Assess for Plasmodium parasites.
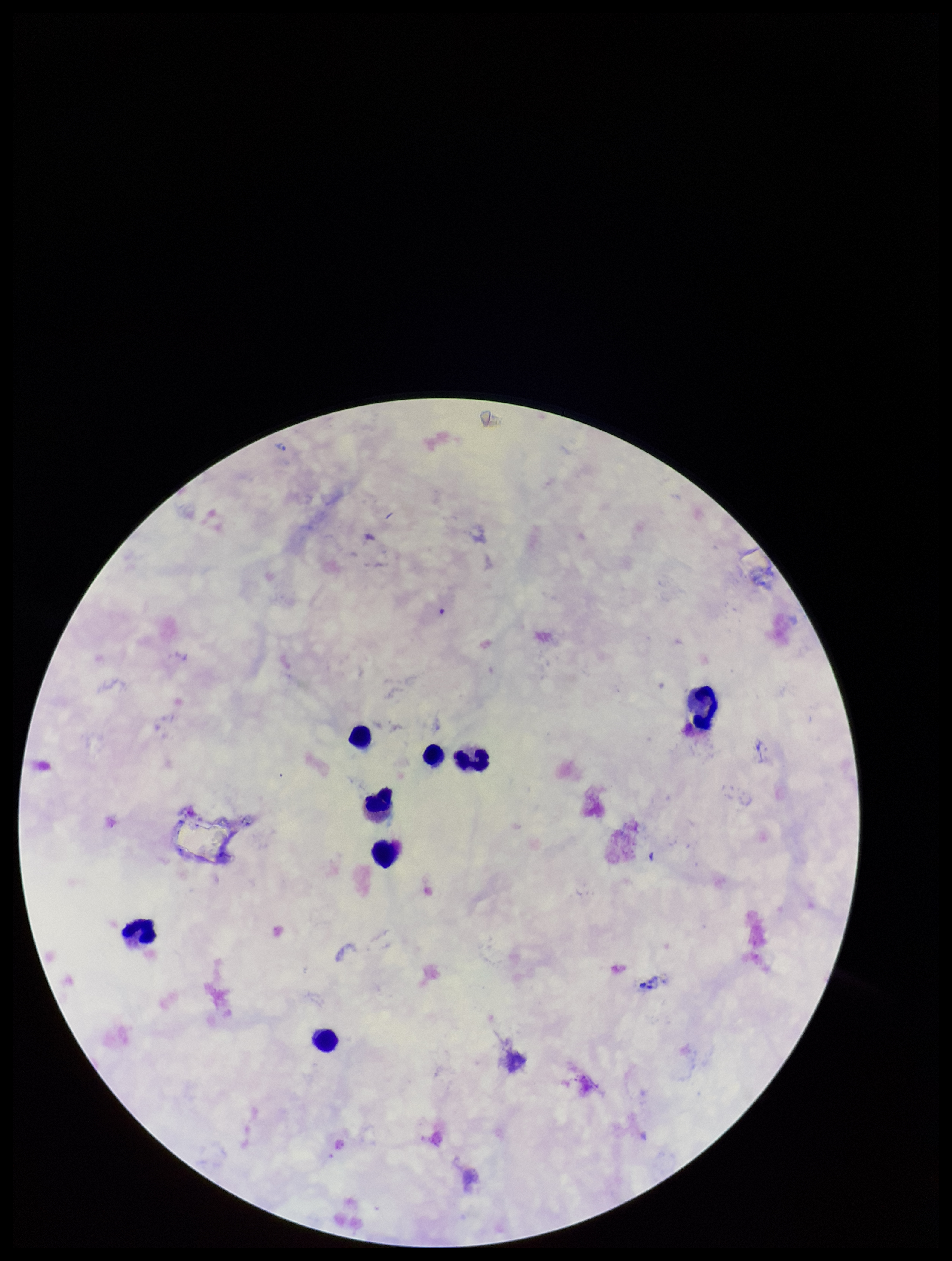

None identified.

Preparation: thick blood smear. Photographed through the microscope eyepiece with a smartphone camera. Single field of view. Image is 952×1261 pixels. Stained with Giemsa. Patient malaria status: positive. Species reported for this patient: Plasmodium falciparum. Leukocyte count: 8. Parasite count: 0.